Assess the morphology of the erythrocytes.
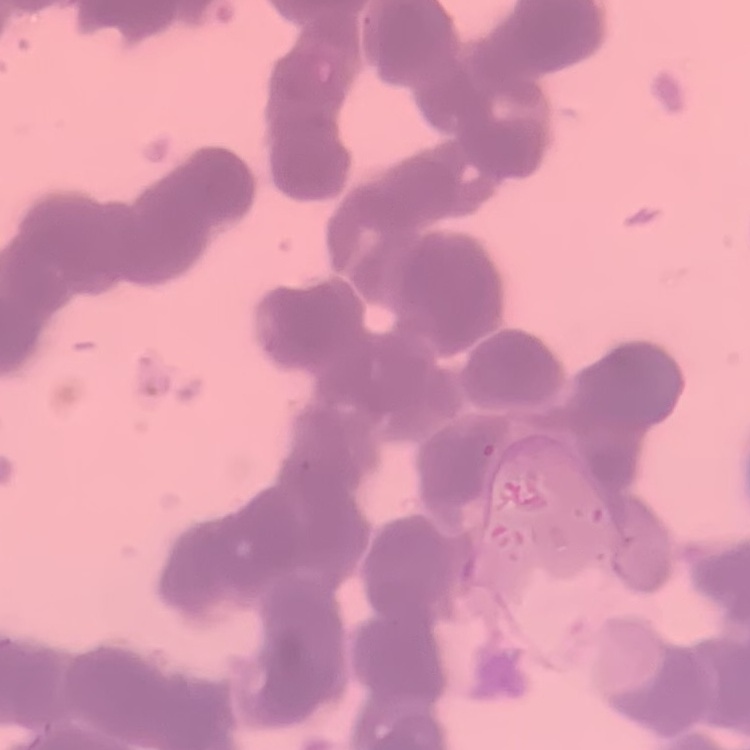
They show rouleaux formation.

Summary:
  - Stain: Field's or Giemsa
  - Image type: one tile cut from a larger photomicrograph
  - Preparation: thin peripheral smear